Name the cell type shown.
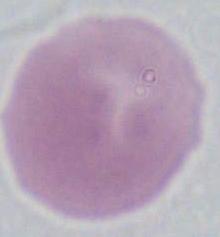
This is an erythrocyte.

magnification: 1000x
modality: photomicrograph